Describe the morphology of the erythrocytes.
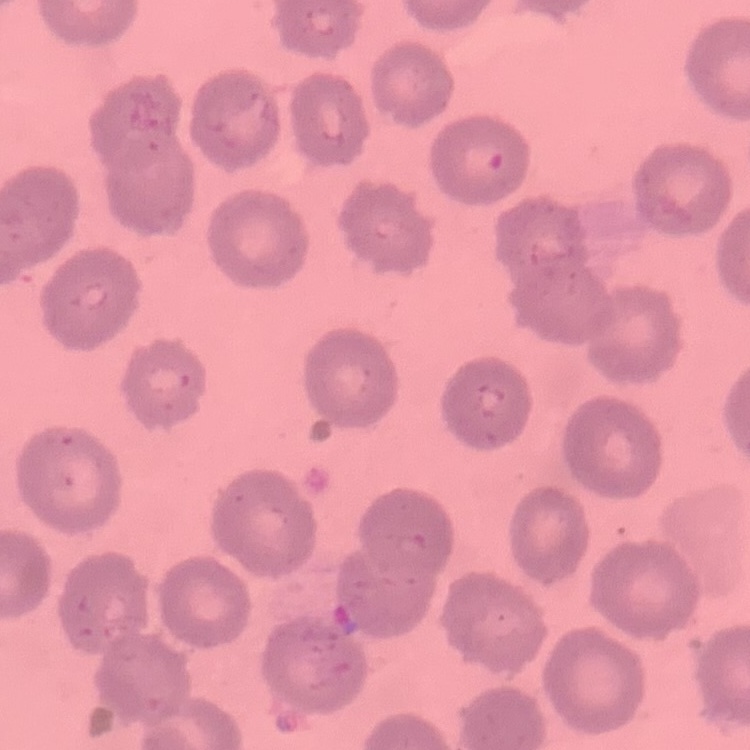
No rouleaux formation.

Thin blood film. Field's or Giemsa stain. Square crop of a larger photomicrograph.